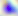
identification: Toxoplasma gondii
modality: photomicrograph
magnification: 400x